Describe the morphology of the erythrocytes.
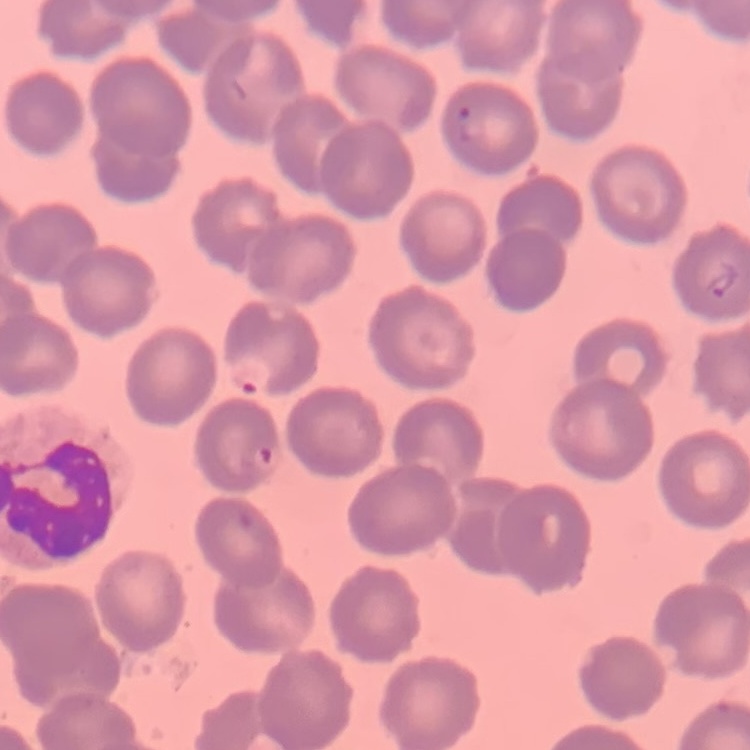
No rouleaux formation.

{
  "preparation": "thin blood smear",
  "stain": "Field's or Giemsa",
  "image_type": "square crop of a larger photomicrograph"
}